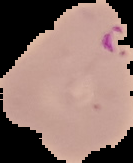
preparation: thin blood film
malaria_status: parasitized
image_size: 133×163 pixels
image_type: segmented cell region on a black background